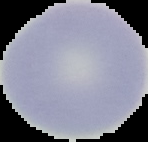
Summary:
  - Image type: segmented cell region with the area outside set to black
  - Malaria status: uninfected
  - Image size: 148×142 pixels
  - Preparation: thin blood smear